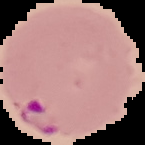

Summary:
  - Image size: 145×145 pixels
  - Preparation: thin blood smear
  - Image type: cell region segmented out of the field of view; surrounding area masked to black
  - Malaria status: parasitized